Assess for Plasmodium parasites.
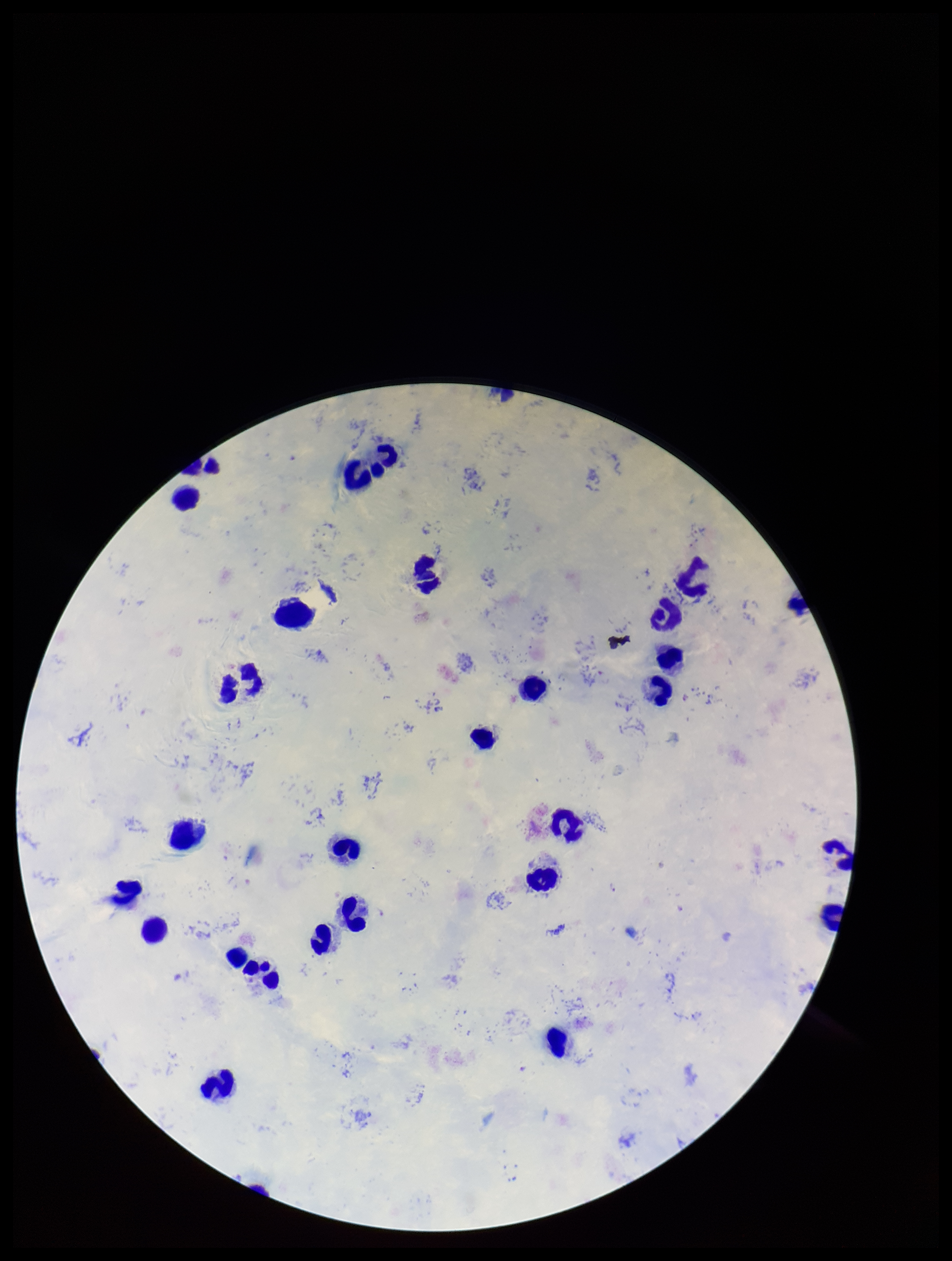
Identified.

capture = smartphone photograph through the microscope eyepiece
leukocyte count = 29
stain = Giemsa
preparation = thick
parasite count = 1
field of view = single
patient malaria status = infected
species reported for this patient = Plasmodium falciparum
image size = 952×1261 pixels